Assess this cell for malaria.
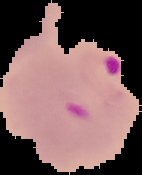
It is parasitized.

Summary:
  - Preparation: thin blood film
  - Image type: segmented cell region on a black background
  - Image size: 142×175 pixels